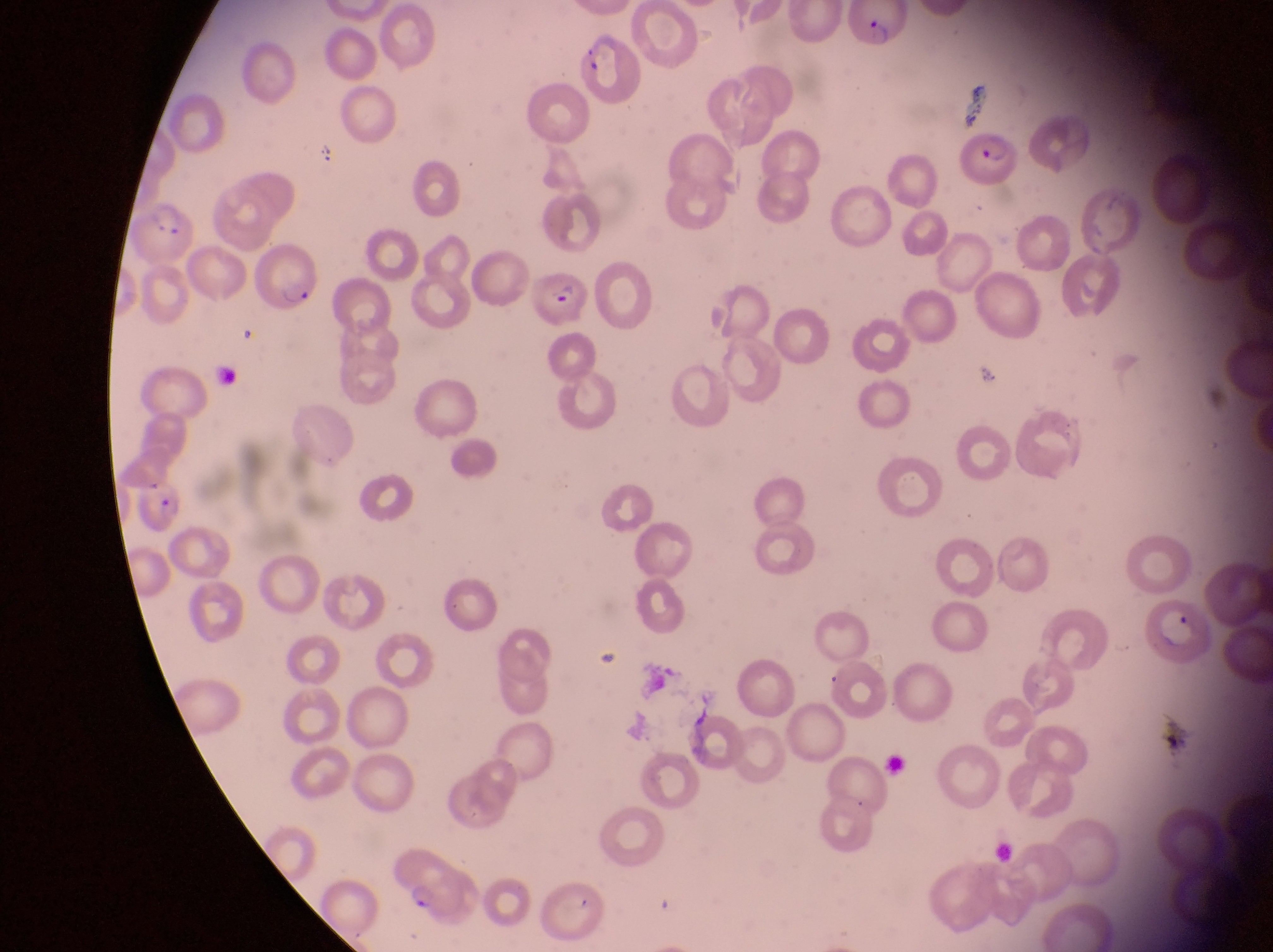
Approximate bounding boxes as {left, top, right, bottom} in pixels. Parasitised red blood cell locations: {852, 4, 907, 50}, {579, 32, 644, 106}, {954, 127, 1023, 187}, {139, 205, 196, 267}, {248, 239, 325, 316}, {532, 270, 594, 330}, {135, 482, 188, 537}, {1141, 592, 1215, 666}, {385, 842, 480, 925}. Image is 1273×952 pixels. Single field of view. Thin blood film. Sample from Uganda. At a magnification of 1000x. Captured by a smartphone held over the eyepiece of an Olympus CX-23 microscope.